Comment on the morphology of the erythrocytes.
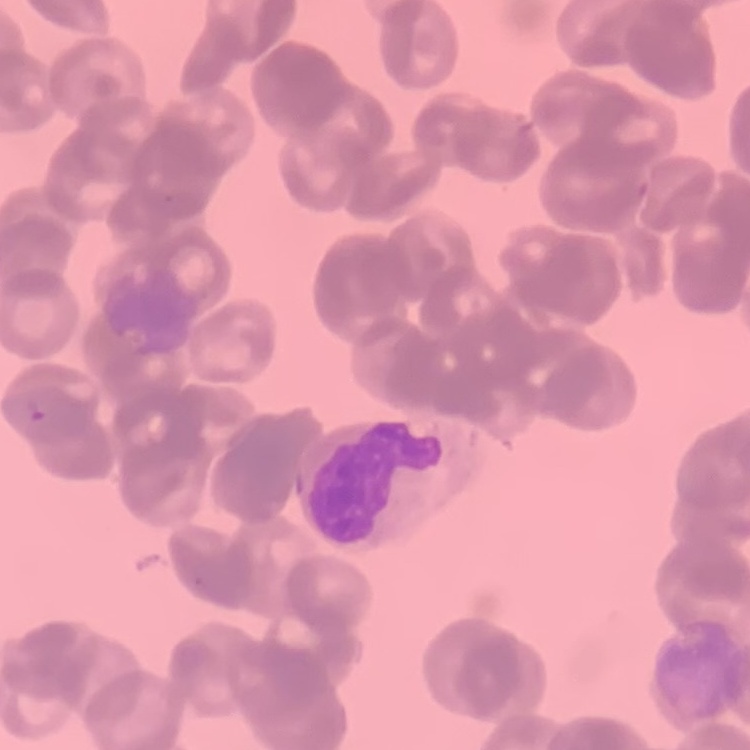

Rouleaux formation.

Thin peripheral smear. Stained with either Field's or Giemsa. One tile cut from a larger photomicrograph.